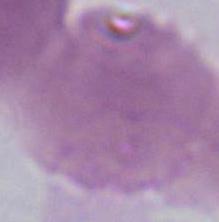
modality = photomicrograph
identification = erythrocyte
magnification = 1000x